Report the malaria status of this cell.
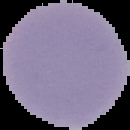

Uninfected.

image_type: cell region segmented out of the field of view; surrounding area masked to black
image_size: 130×130 pixels
preparation: thin blood smear